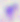

Summary:
  - Identification: Toxoplasma gondii
  - Modality: photomicrograph
  - Magnification: 400x